Locate every Plasmodium parasite.
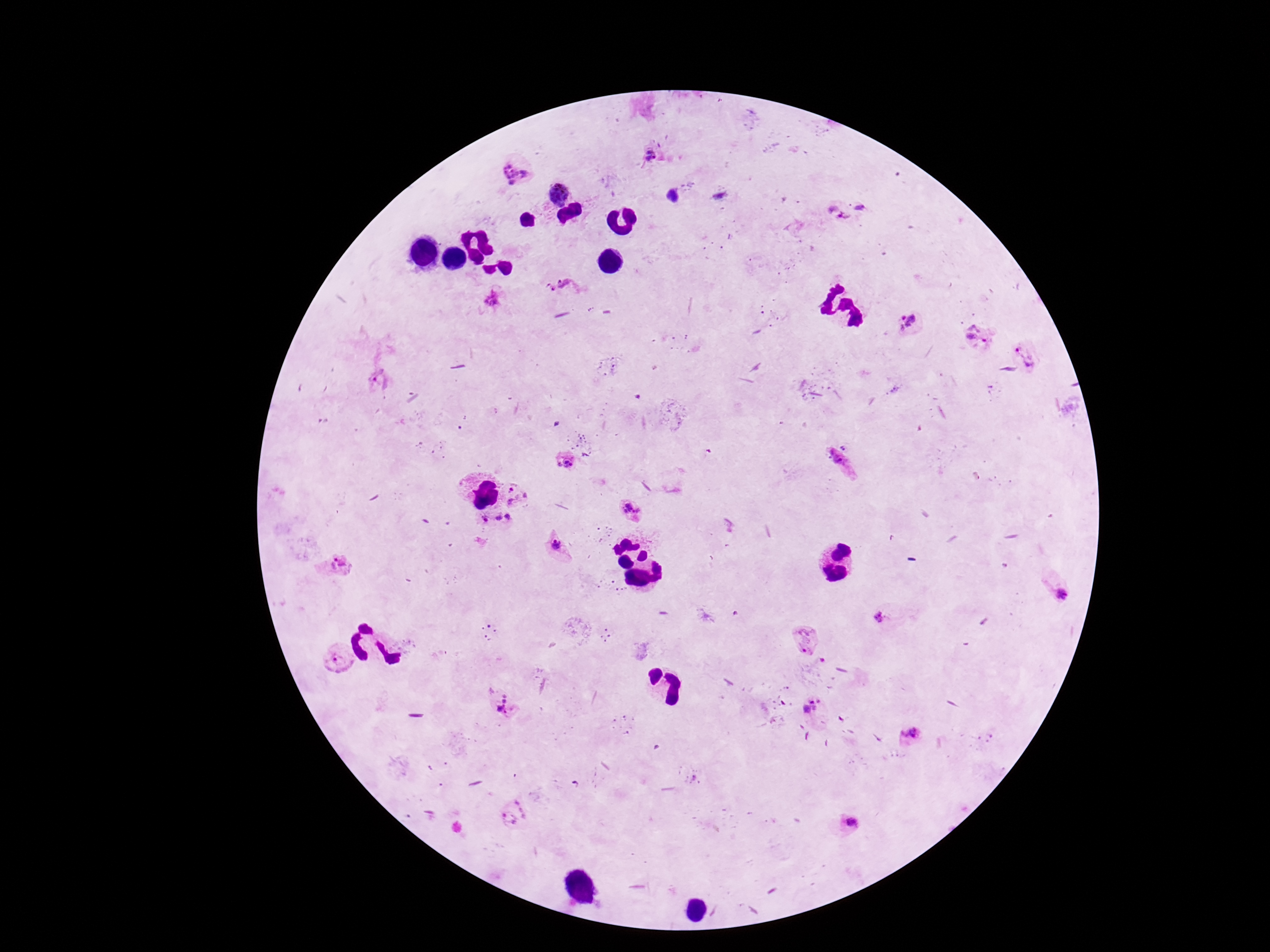

Approximate centers as [x, y] in pixels.
Plasmodium parasites: [650, 154], [514, 173], [557, 192], [861, 207], [837, 216], [566, 289], [492, 299], [909, 322], [979, 337], [1024, 354], [375, 377], [843, 461], [564, 462], [516, 495], [631, 507], [498, 517], [508, 517], [484, 519], [557, 545], [340, 566], [1058, 593], [881, 616], [805, 640], [339, 658], [506, 703], [811, 707], [911, 735], [511, 815], [849, 825].

Summary:
  - Image size: 1270×952 pixels
  - Capture: smartphone camera through the microscope eyepiece
  - Field of view: single
  - Stain: Giemsa
  - Preparation: thick blood smear
  - Magnification: 100x
  - Patient malaria status: infected